Point out each malaria parasite.
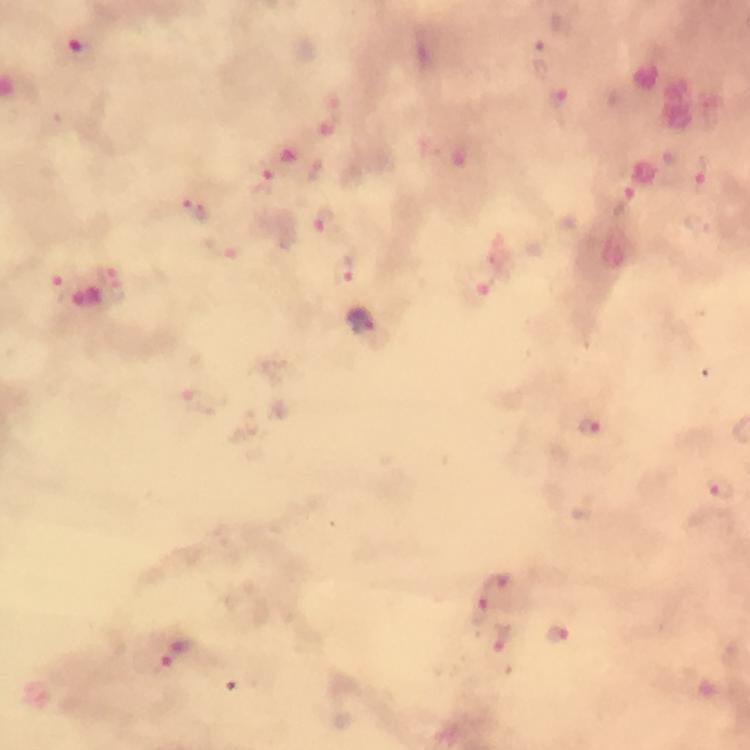
Approximate centers as {x, y} in pixels.
Malaria parasites: {76, 51}, {559, 102}, {315, 169}, {702, 174}, {265, 176}, {196, 209}, {324, 220}, {107, 268}, {344, 269}, {60, 290}, {362, 319}, {590, 426}, {718, 489}, {509, 588}, {480, 611}, {558, 634}, {503, 643}, {176, 652}.

{
  "preparation": "thick smear",
  "capture": "smartphone camera through the microscope",
  "image_size": "750×750 pixels",
  "stain": "Giemsa",
  "immersion_oil": "applied",
  "cropped_from": "a single field of view",
  "magnification": "100x",
  "context": "from a malaria diagnostic workup"
}